Evaluate for malaria.
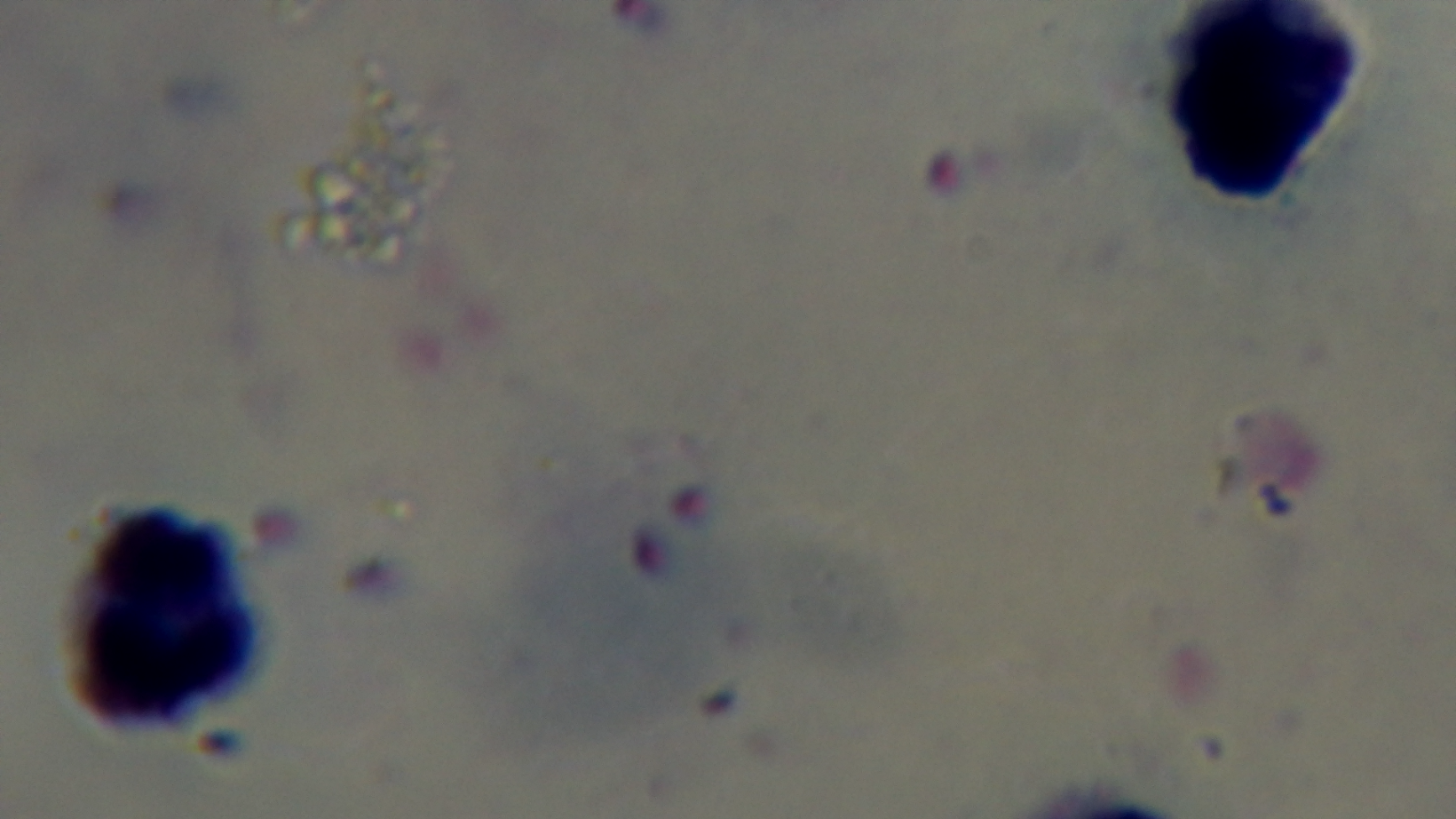

It is infected.

Summary:
  - Stain: Giemsa
  - Capture: mounted 4K digital camera
  - Objective: 100x oil immersion
  - Field of view: single
  - Preparation: thick blood film
  - Modality: light microscopy